Identify the cell.
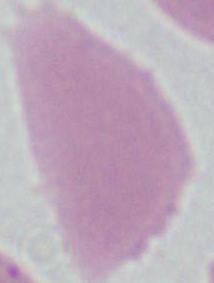
This is an erythrocyte.

Summary:
  - Modality: photomicrograph
  - Magnification: 1000x